Identify the blood parasite species.
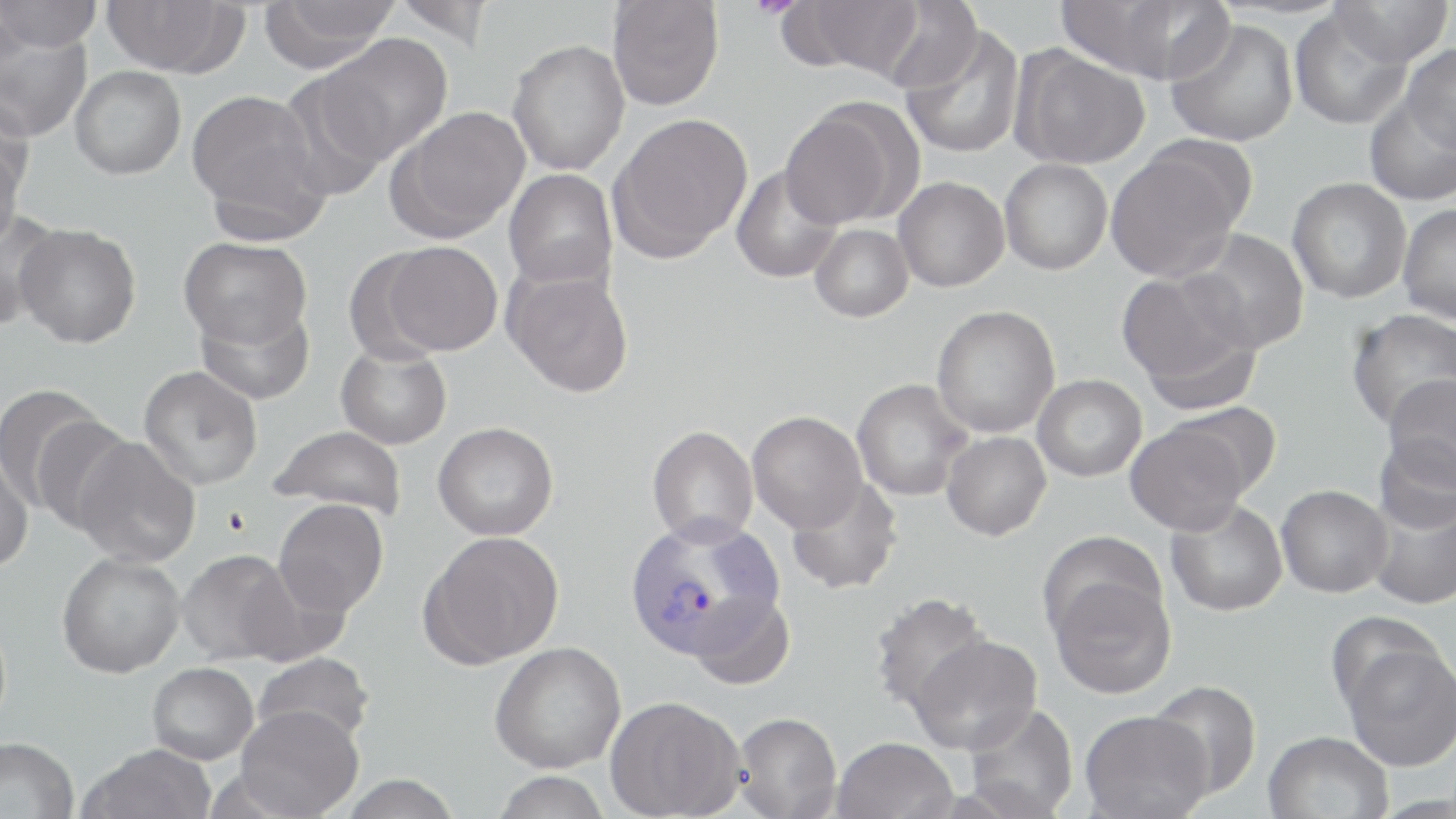
Plasmodium vivax.

{
  "field_of_view": "one of a larger specimen",
  "magnification": "1000x",
  "modality": "optical microscopy",
  "preparation": "thin blood film",
  "uninfected_red_blood_cell_locations": "approximate bounding boxes as named x1/y1/x2/y2 corners in pixels: (x1=0, y1=0, x2=103, y2=53), (x1=100, y1=0, x2=248, y2=77), (x1=390, y1=0, x2=495, y2=47), (x1=782, y1=0, x2=926, y2=80), (x1=258, y1=1, x2=400, y2=72), (x1=607, y1=1, x2=724, y2=111), (x1=877, y1=1, x2=983, y2=95), (x1=1060, y1=1, x2=1229, y2=83), (x1=1330, y1=1, x2=1453, y2=66), (x1=1290, y1=7, x2=1412, y2=131), (x1=1165, y1=17, x2=1298, y2=147), (x1=899, y1=24, x2=1026, y2=159), (x1=1, y1=25, x2=93, y2=143), (x1=317, y1=34, x2=453, y2=164), (x1=507, y1=39, x2=629, y2=175), (x1=1402, y1=42, x2=1456, y2=154), (x1=1010, y1=46, x2=1150, y2=170), (x1=70, y1=66, x2=186, y2=180), (x1=276, y1=71, x2=393, y2=201), (x1=187, y1=89, x2=329, y2=237), (x1=1363, y1=89, x2=1456, y2=207), (x1=778, y1=101, x2=909, y2=230), (x1=387, y1=106, x2=530, y2=242), (x1=608, y1=113, x2=753, y2=262), (x1=0, y1=139, x2=25, y2=254), (x1=1105, y1=147, x2=1246, y2=282), (x1=1000, y1=159, x2=1113, y2=275), (x1=730, y1=165, x2=842, y2=283), (x1=504, y1=169, x2=618, y2=289), (x1=893, y1=177, x2=1010, y2=292), (x1=1287, y1=178, x2=1412, y2=304), (x1=1397, y1=204, x2=1456, y2=324), (x1=0, y1=211, x2=60, y2=331), (x1=15, y1=223, x2=141, y2=348), (x1=810, y1=224, x2=913, y2=322), (x1=1185, y1=229, x2=1310, y2=353), (x1=179, y1=236, x2=312, y2=350), (x1=376, y1=241, x2=503, y2=356), (x1=503, y1=268, x2=635, y2=397), (x1=1116, y1=270, x2=1260, y2=410), (x1=195, y1=298, x2=315, y2=405), (x1=932, y1=305, x2=1060, y2=437), (x1=1345, y1=309, x2=1456, y2=431), (x1=336, y1=343, x2=452, y2=449), (x1=138, y1=366, x2=263, y2=489), (x1=1032, y1=374, x2=1147, y2=482), (x1=1382, y1=375, x2=1455, y2=489), (x1=851, y1=379, x2=973, y2=501), (x1=0, y1=383, x2=111, y2=516), (x1=1166, y1=401, x2=1283, y2=499), (x1=747, y1=411, x2=866, y2=532), (x1=30, y1=413, x2=138, y2=535), (x1=1125, y1=419, x2=1253, y2=535), (x1=433, y1=421, x2=559, y2=540), (x1=269, y1=425, x2=407, y2=521), (x1=647, y1=425, x2=758, y2=546), (x1=942, y1=431, x2=1051, y2=541), (x1=1374, y1=435, x2=1456, y2=532), (x1=71, y1=436, x2=201, y2=568), (x1=0, y1=451, x2=33, y2=574), (x1=785, y1=476, x2=904, y2=596), (x1=1276, y1=485, x2=1393, y2=597), (x1=1366, y1=492, x2=1456, y2=610), (x1=273, y1=498, x2=389, y2=617), (x1=1166, y1=499, x2=1287, y2=617), (x1=420, y1=531, x2=565, y2=668), (x1=1037, y1=531, x2=1166, y2=641), (x1=177, y1=549, x2=303, y2=666), (x1=56, y1=552, x2=185, y2=678), (x1=1048, y1=572, x2=1176, y2=699), (x1=688, y1=590, x2=794, y2=691), (x1=869, y1=592, x2=993, y2=717), (x1=908, y1=633, x2=1043, y2=755), (x1=1338, y1=636, x2=1456, y2=772), (x1=489, y1=641, x2=627, y2=773), (x1=252, y1=652, x2=373, y2=749), (x1=147, y1=662, x2=258, y2=764), (x1=1148, y1=679, x2=1262, y2=800), (x1=605, y1=695, x2=745, y2=819), (x1=963, y1=702, x2=1079, y2=818), (x1=234, y1=705, x2=364, y2=818), (x1=1079, y1=710, x2=1213, y2=819), (x1=732, y1=711, x2=842, y2=818), (x1=1263, y1=730, x2=1394, y2=819), (x1=0, y1=736, x2=79, y2=819), (x1=832, y1=736, x2=958, y2=819), (x1=78, y1=744, x2=217, y2=819), (x1=489, y1=771, x2=613, y2=819), (x1=337, y1=774, x2=462, y2=818)",
  "stain": "May-Grünwald-Giemsa",
  "plasmodium_vivax_infected_red_blood_cell_locations": "approximate bounding boxes as named x1/y1/x2/y2 corners in pixels: (x1=623, y1=515, x2=782, y2=660)",
  "image_size": "1456×819 pixels"
}